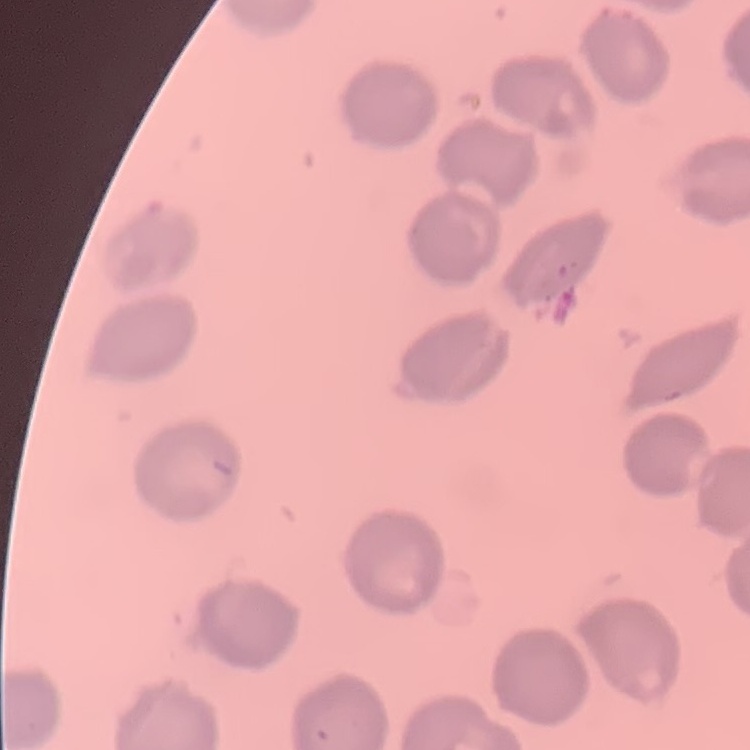
erythrocyte morphology = no rouleaux formation
stain = Field's or Giemsa
image type = one tile cut from a larger photomicrograph
preparation = thin peripheral smear